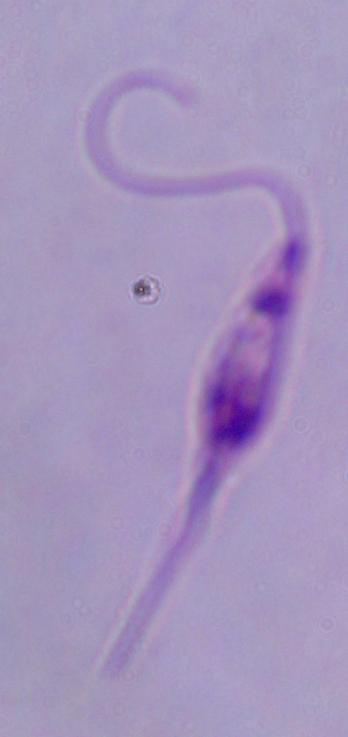

A Leishmania parasite is seen. Captured at 1000x magnification. Micrograph.